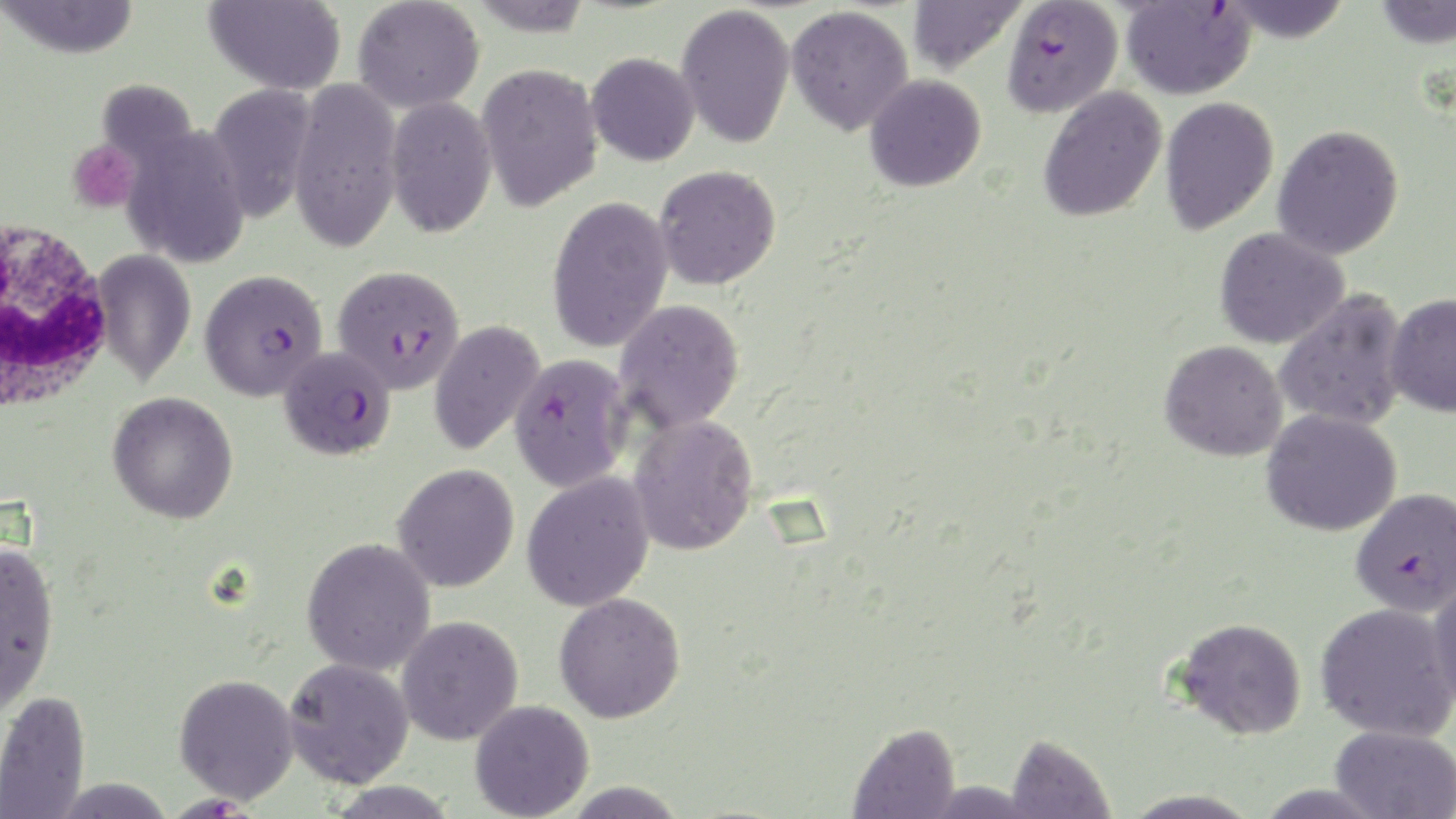
Summary:
  - Coordinate format: approximate bounding boxes as (x1, y1, x2, y2) in pixels
  - Uninfected red blood cell locations: (2, 0, 140, 59), (204, 0, 346, 95), (352, 0, 484, 113), (467, 0, 594, 37), (907, 0, 1026, 76), (1217, 0, 1355, 42), (1373, 0, 1456, 49), (676, 3, 795, 149), (786, 5, 913, 136), (586, 52, 699, 166), (476, 62, 604, 212), (864, 74, 986, 192), (288, 79, 403, 252), (207, 83, 317, 224), (1038, 87, 1168, 223), (385, 96, 497, 238), (1159, 96, 1280, 235), (1272, 124, 1405, 260), (124, 125, 249, 268), (654, 164, 781, 289), (547, 195, 674, 353), (1214, 227, 1350, 349), (93, 249, 195, 388), (1274, 289, 1411, 432), (1385, 292, 1456, 418), (614, 299, 745, 434), (428, 318, 545, 456), (1159, 339, 1289, 462), (108, 391, 239, 524), (1262, 409, 1402, 536), (627, 414, 759, 557), (392, 463, 520, 592), (521, 471, 655, 612), (301, 537, 436, 676), (0, 541, 60, 713), (1428, 576, 1456, 714), (553, 592, 686, 723), (1315, 603, 1455, 741), (396, 615, 524, 745), (1173, 616, 1307, 740), (283, 657, 415, 788), (173, 673, 299, 804), (0, 690, 91, 818), (469, 700, 594, 819), (848, 721, 962, 818), (1330, 725, 1456, 819), (1004, 733, 1115, 818), (559, 780, 690, 817)
  - Platelet locations: (66, 139, 141, 213)
  - Plasmodium falciparum-infected red blood cell locations: (1002, 0, 1123, 117), (1120, 1, 1256, 100), (332, 264, 464, 394), (200, 268, 328, 401), (279, 345, 396, 461), (508, 352, 632, 493), (1350, 488, 1456, 616), (169, 788, 255, 819)
  - White blood cell locations: (0, 216, 115, 415)
  - Slide-level diagnosis: Plasmodium falciparum
  - Modality: optical microscopy
  - Image size: 1456×819 pixels
  - Magnification: 1000x
  - Field of view: single
  - Stain: May-Grünwald-Giemsa
  - Preparation: thin blood smear